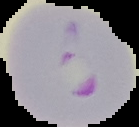

result: Plasmodium parasites detected
image_type: segmented cell region with the area outside set to black
preparation: thin blood smear
image_size: 139×127 pixels